Point out each malaria parasite.
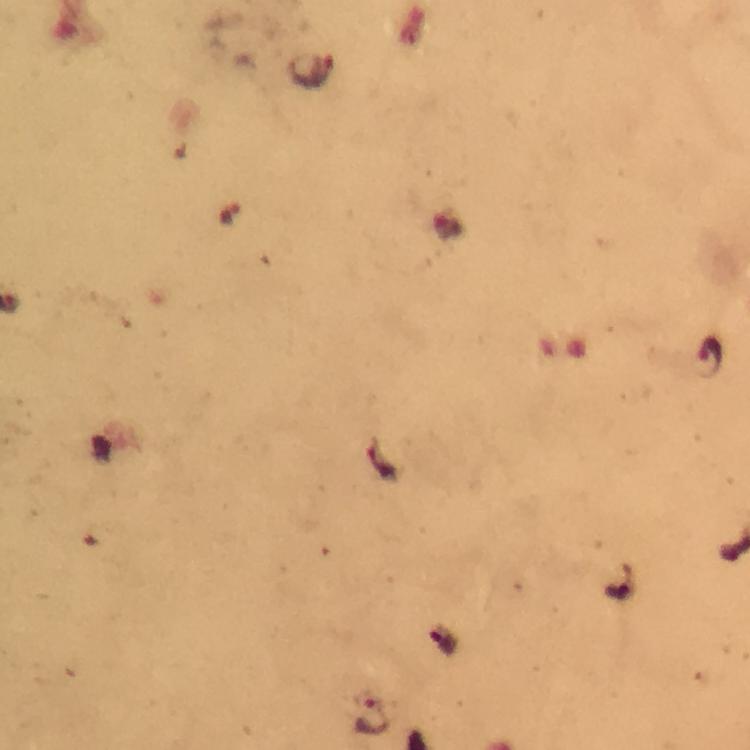
Approximate centers as (x, y) in pixels.
Malaria parasites: (312, 72), (711, 358), (367, 716).

{
  "image_size": "750×750 pixels",
  "magnification": "100x",
  "capture": "smartphone mounted on the microscope",
  "cropped_from": "a single field of view",
  "preparation": "thick blood film",
  "immersion_oil": "applied",
  "context": "from a malaria diagnostic workup",
  "stain": "Giemsa"
}